Outline each Plasmodium falciparum-infected red blood cell.
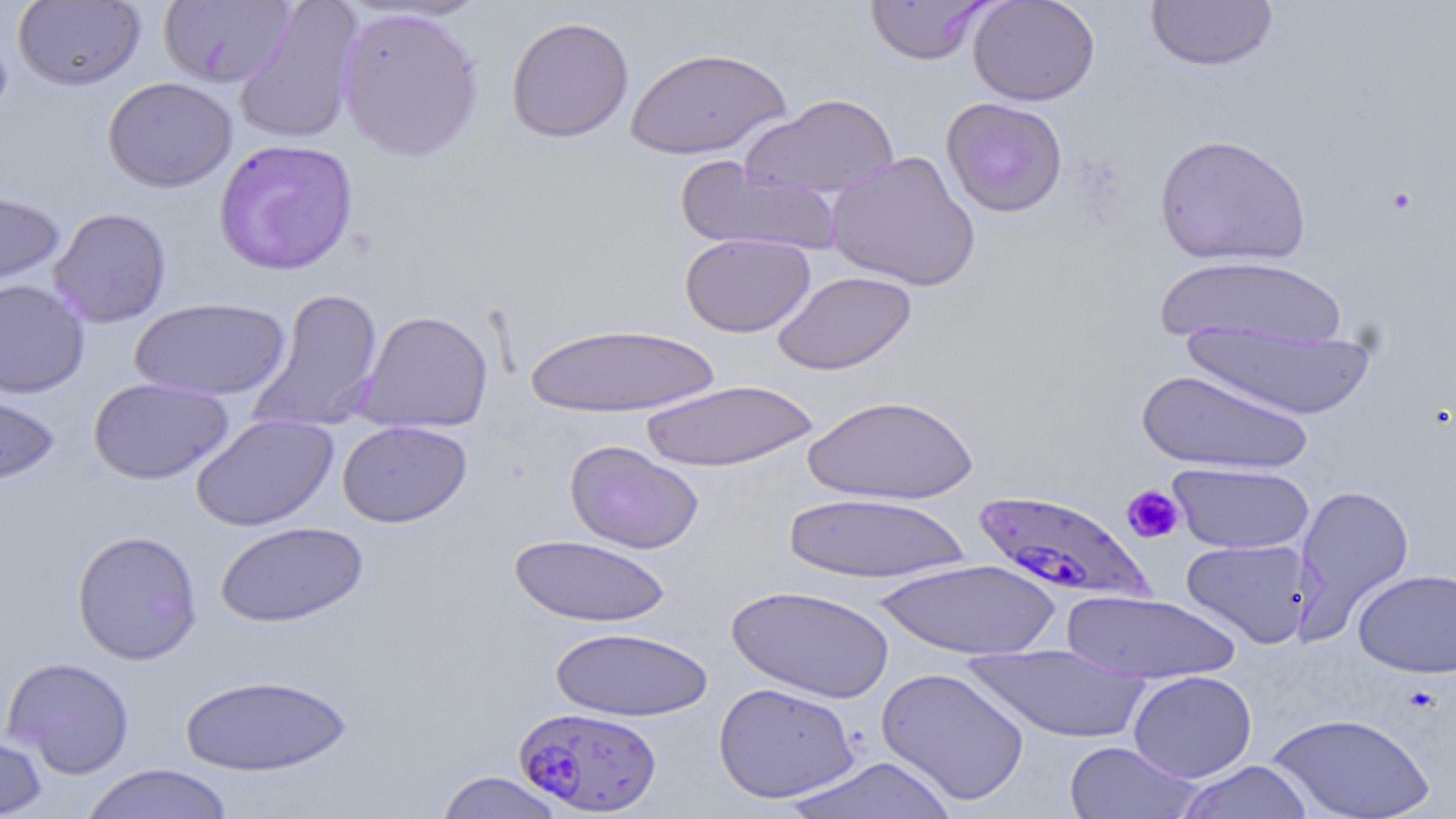

Approximate bounding boxes as named x1/y1/x2/y2 corners in pixels.
Plasmodium falciparum-infected red blood cells: (x1=970, y1=488, x2=1156, y2=605), (x1=514, y1=706, x2=663, y2=816).

Uninfected red blood cell locations: (x1=968, y1=0, x2=1100, y2=106), (x1=1145, y1=0, x2=1279, y2=72), (x1=13, y1=1, x2=146, y2=91), (x1=159, y1=1, x2=295, y2=87), (x1=864, y1=1, x2=996, y2=66), (x1=234, y1=2, x2=364, y2=146), (x1=336, y1=6, x2=485, y2=162), (x1=505, y1=16, x2=634, y2=143), (x1=625, y1=46, x2=791, y2=160), (x1=103, y1=77, x2=238, y2=192), (x1=741, y1=93, x2=901, y2=199), (x1=940, y1=97, x2=1069, y2=217), (x1=1153, y1=132, x2=1312, y2=267), (x1=213, y1=138, x2=359, y2=276), (x1=826, y1=151, x2=981, y2=292), (x1=675, y1=157, x2=842, y2=257), (x1=0, y1=187, x2=66, y2=291), (x1=48, y1=207, x2=172, y2=328), (x1=679, y1=233, x2=815, y2=337), (x1=1154, y1=255, x2=1349, y2=350), (x1=771, y1=270, x2=917, y2=376), (x1=0, y1=278, x2=90, y2=398), (x1=248, y1=286, x2=385, y2=434), (x1=130, y1=296, x2=291, y2=401), (x1=357, y1=309, x2=494, y2=433), (x1=523, y1=322, x2=721, y2=417), (x1=1180, y1=322, x2=1379, y2=420), (x1=1136, y1=368, x2=1312, y2=473), (x1=88, y1=377, x2=234, y2=485), (x1=639, y1=379, x2=819, y2=471), (x1=0, y1=386, x2=60, y2=488), (x1=802, y1=393, x2=979, y2=505), (x1=191, y1=413, x2=338, y2=532), (x1=337, y1=420, x2=472, y2=528), (x1=564, y1=440, x2=704, y2=554), (x1=1167, y1=462, x2=1314, y2=554), (x1=1293, y1=484, x2=1415, y2=636), (x1=783, y1=492, x2=973, y2=584), (x1=215, y1=520, x2=369, y2=628), (x1=72, y1=529, x2=203, y2=665), (x1=508, y1=534, x2=671, y2=628), (x1=1180, y1=538, x2=1314, y2=649), (x1=875, y1=559, x2=1061, y2=660), (x1=1353, y1=568, x2=1456, y2=678), (x1=726, y1=584, x2=895, y2=704), (x1=1062, y1=590, x2=1242, y2=685), (x1=549, y1=626, x2=714, y2=722), (x1=965, y1=645, x2=1151, y2=744), (x1=2, y1=656, x2=136, y2=779), (x1=876, y1=666, x2=1030, y2=806), (x1=1128, y1=670, x2=1257, y2=782), (x1=179, y1=674, x2=353, y2=777), (x1=712, y1=681, x2=861, y2=804), (x1=1267, y1=712, x2=1435, y2=819), (x1=0, y1=730, x2=48, y2=819), (x1=1063, y1=741, x2=1202, y2=818), (x1=783, y1=756, x2=957, y2=818), (x1=1173, y1=759, x2=1315, y2=818), (x1=79, y1=763, x2=235, y2=819), (x1=434, y1=770, x2=565, y2=819). Platelet locations: (x1=1121, y1=485, x2=1185, y2=544). Slide-level diagnosis: Plasmodium falciparum. Thin blood smear. Image is 1456×819 pixels. May-Grünwald-Giemsa-stained preparation. Captured at 1000x magnification. Light microscopy. Single field of view.